Assess the morphology of the red blood cells.
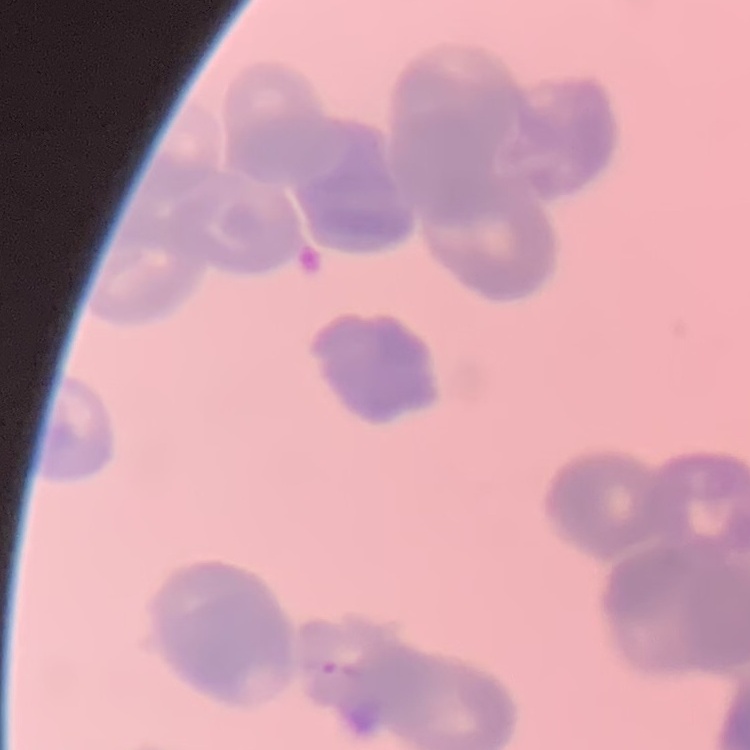
Rouleaux formation.

One tile cut from a larger photomicrograph. Stained with either Field's or Giemsa. Thin blood smear.